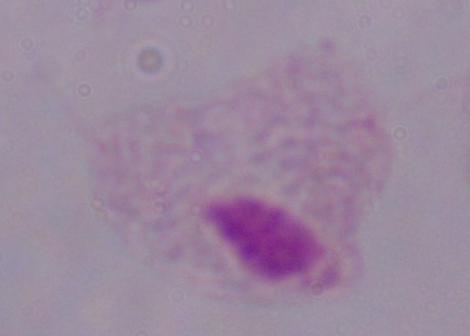

Summary:
  - Identification: trichomonad
  - Magnification: 1000x
  - Modality: micrograph